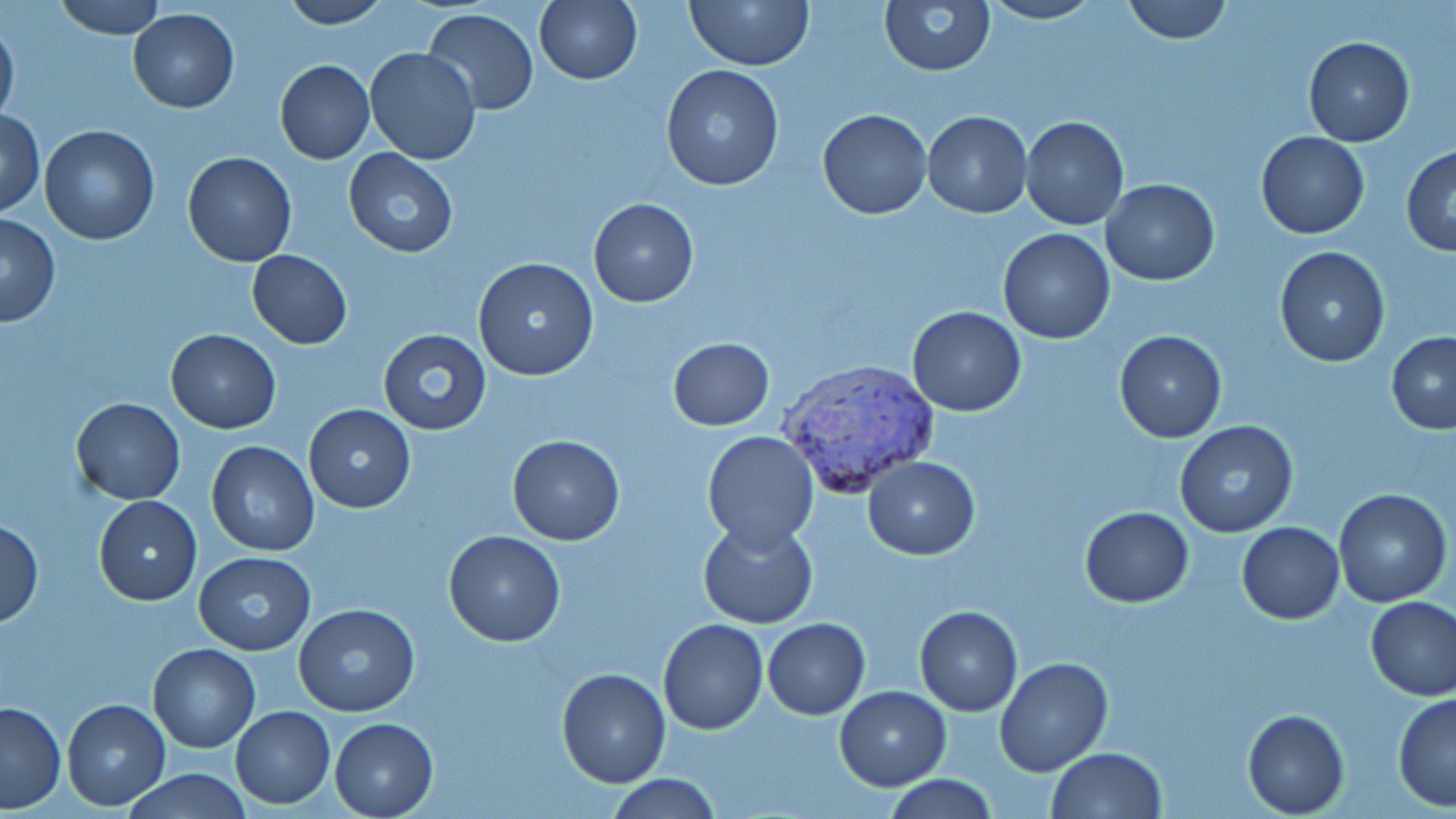

Summary:
  - Coordinate format: approximate bounding boxes as (x1,y1)-(x2,y2) corner pairs in pixels
  - Uninfected red blood cell locations: (55,0)-(165,39), (278,0)-(391,28), (535,0)-(642,85), (686,0)-(813,69), (877,0)-(996,77), (1120,0)-(1233,44), (979,1)-(1104,25), (129,8)-(239,112), (422,8)-(539,115), (0,16)-(20,127), (1304,36)-(1415,147), (364,47)-(482,164), (274,59)-(374,164), (661,64)-(783,192), (2,108)-(45,215), (818,108)-(931,220), (922,110)-(1032,218), (1020,114)-(1129,231), (39,124)-(160,245), (1256,131)-(1369,239), (1402,145)-(1456,255), (344,148)-(458,258), (183,151)-(297,267), (1100,178)-(1220,285), (587,197)-(698,307), (0,214)-(60,327), (998,229)-(1115,344), (1273,245)-(1392,367), (247,250)-(352,348), (473,257)-(600,381), (907,306)-(1027,417), (165,328)-(281,433), (378,329)-(490,436), (1114,330)-(1226,443), (1386,330)-(1456,434), (667,337)-(774,431), (71,397)-(185,505), (303,404)-(416,514), (1172,421)-(1298,539), (700,431)-(819,550), (507,434)-(627,546), (206,441)-(318,555), (864,456)-(980,559), (1334,488)-(1450,607), (93,496)-(202,605), (1079,506)-(1194,608), (0,517)-(42,628), (697,518)-(819,629), (1237,521)-(1345,624), (443,529)-(565,647), (192,552)-(316,656), (1365,596)-(1456,702), (293,603)-(420,715), (914,605)-(1023,716), (762,618)-(870,719), (658,619)-(769,735), (148,643)-(260,754), (993,657)-(1111,776), (556,667)-(671,788), (834,685)-(951,790), (1392,692)-(1456,812), (61,698)-(170,811), (0,701)-(66,814), (230,706)-(336,808), (1243,710)-(1349,817), (330,717)-(439,817), (1047,747)-(1166,819), (122,768)-(253,819), (607,774)-(722,818), (884,776)-(998,818)
  - Plasmodium vivax-infected red blood cell locations: (780,359)-(942,495)
  - Slide-level diagnosis: Plasmodium vivax
  - Stain: May-Grünwald-Giemsa
  - Preparation: thin blood smear
  - Image size: 1456×819 pixels
  - Field of view: single
  - Magnification: 1000x
  - Modality: light microscopy